Find each parasitized RBC.
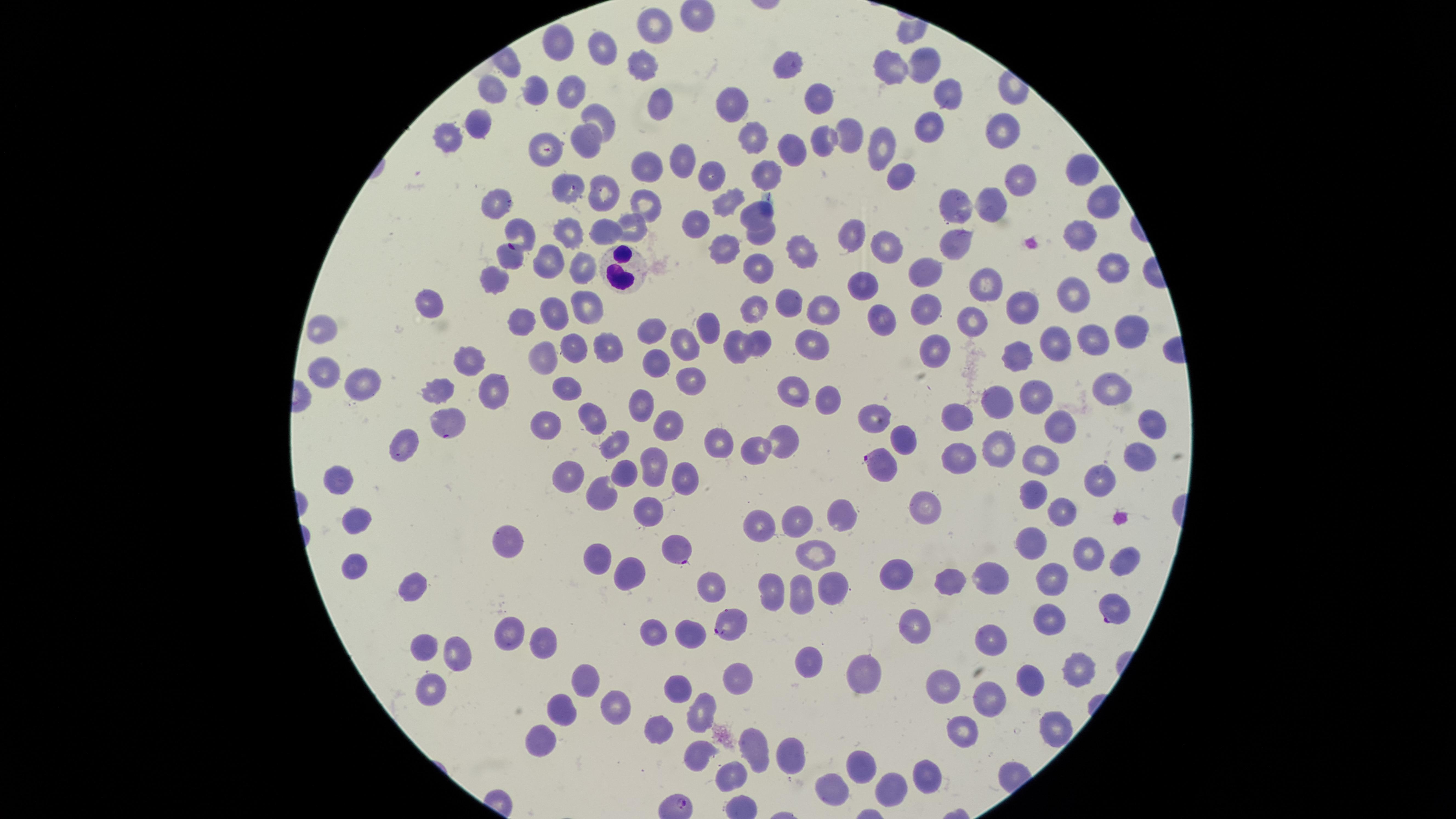
Approximate marker points as (x, y) in pixels.
Parasitized RBCs: (519, 233), (882, 459), (676, 553), (1115, 612), (730, 623).

Approximate marker points as (x, y) in pixels.
Summary:
  - WBCs: (623, 269)
  - Uninfected RBCs: (653, 24), (555, 44), (599, 47), (920, 59), (788, 65), (892, 66), (638, 70), (493, 88), (569, 88), (534, 89), (952, 90), (657, 98), (818, 98), (726, 100), (596, 113), (479, 120), (925, 121), (1010, 125), (444, 131), (849, 134), (748, 139), (824, 140), (588, 141), (878, 145), (791, 147), (541, 149), (677, 154), (646, 165), (766, 165), (1083, 167), (706, 170), (904, 171), (1017, 178), (564, 186), (600, 192), (646, 198), (724, 199), (501, 202), (957, 204), (1098, 205), (991, 206), (751, 209), (697, 215), (629, 225), (567, 226), (607, 227), (756, 229), (849, 231), (1076, 235), (883, 245), (721, 248), (951, 248), (807, 252), (509, 260), (582, 260), (547, 262), (1108, 264), (928, 265), (760, 268), (498, 280), (863, 280), (991, 280), (1071, 291), (429, 298), (791, 301), (754, 305), (1024, 306), (584, 307), (820, 307), (922, 307), (552, 311), (879, 314), (973, 320), (709, 322), (526, 323), (650, 328), (1129, 336), (684, 338), (760, 339), (1051, 339), (1091, 339), (813, 340), (574, 344), (932, 345), (600, 346), (733, 348), (547, 350), (1017, 351), (656, 357), (469, 360), (325, 370), (692, 374), (361, 380), (1114, 382), (569, 384), (493, 387), (438, 391), (790, 391), (825, 393), (1037, 395), (998, 400), (641, 401), (962, 414), (591, 415), (873, 415), (550, 417), (671, 417), (446, 419), (1057, 422), (1148, 423), (785, 431), (709, 434), (902, 435), (615, 439), (402, 441), (997, 446), (752, 448), (1043, 451), (1137, 453), (955, 454), (650, 464), (572, 473), (1100, 474), (674, 475), (625, 477), (334, 479), (605, 487), (1036, 497), (647, 506), (922, 506), (1065, 512), (840, 516), (805, 517), (360, 524), (761, 524), (519, 538), (1031, 540), (1087, 550), (810, 554), (595, 557), (1121, 558), (631, 564), (354, 567), (900, 574), (1052, 575), (990, 577), (410, 578), (954, 581), (708, 582), (822, 588), (770, 589), (796, 593), (1048, 616), (913, 621), (650, 629), (687, 629), (510, 633), (544, 637), (994, 638), (423, 644), (461, 652), (811, 658), (1074, 666), (585, 669), (1030, 677), (733, 678), (872, 679), (679, 684), (432, 686), (942, 686), (994, 695), (701, 706), (563, 710), (611, 710), (660, 725), (1050, 728), (958, 729), (793, 746), (544, 747), (754, 750), (699, 753), (864, 765), (926, 775), (732, 776), (833, 783), (890, 784)
  - Field of view: single
  - Capture: smartphone photograph through the microscope eyepiece
  - Preparation: thin smear of blood
  - Image size: 1456×819 pixels
  - Species: Plasmodium falciparum
  - Stain: Giemsa
  - Visible region: circular